Classify this cell by malaria status.
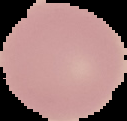

Uninfected.

Summary:
  - Image size: 127×121 pixels
  - Image type: cell region segmented out of the field of view; surrounding area masked to black
  - Preparation: thin blood film